Comment on the morphology of the erythrocytes.
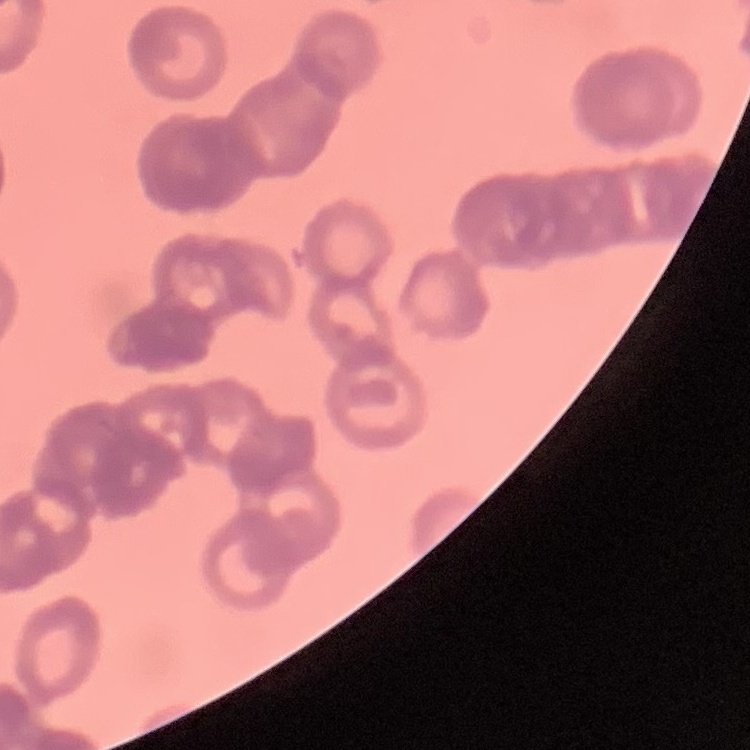
They show rouleaux formation.

One tile cut from a larger photomicrograph. Field's or Giemsa stain. Thin blood smear.